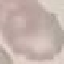

Summary:
  - Malaria status: uninfected
  - Capture: smartphone camera at the microscope eyepiece
  - Stain: Giemsa
  - Preparation: thin blood smear
  - Image type: automatically extracted cell patch, resized to 64 × 64 pixels